Assess the morphology of the red blood cells.
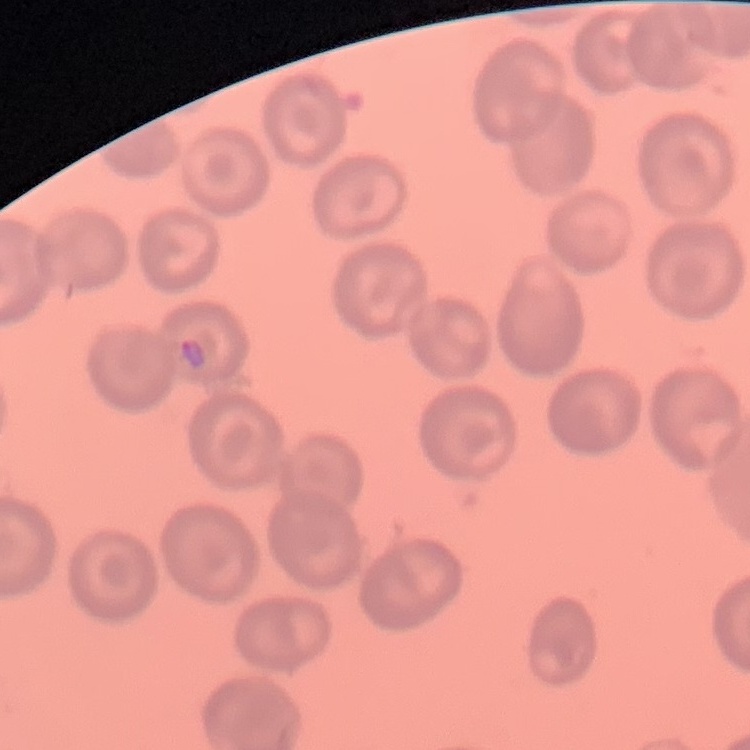
They show no rouleaux formation.

Summary:
  - Image type: square crop of a larger photomicrograph
  - Preparation: thin blood film
  - Stain: Field's or Giemsa